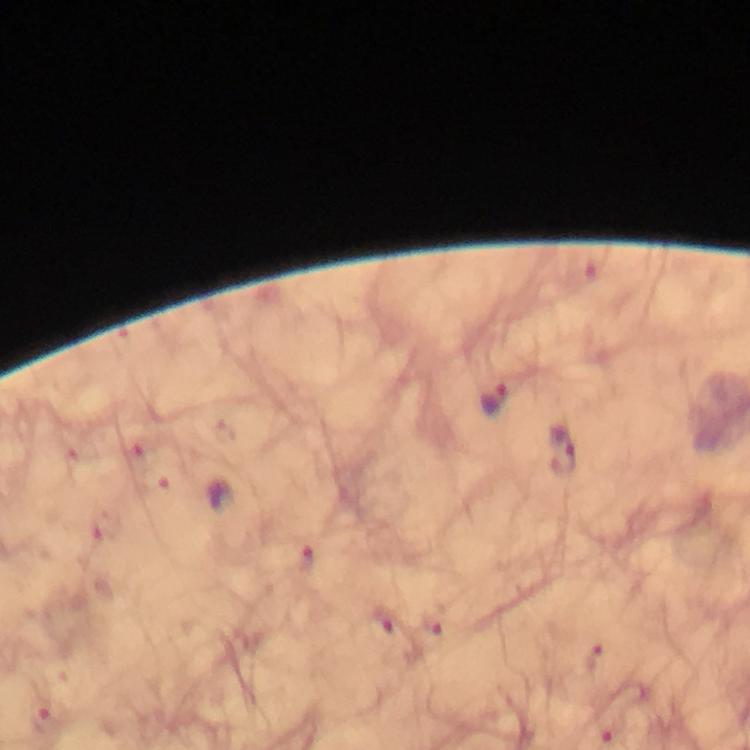

Approximate centers as (x, y) in pixels.
Summary:
  - Malaria parasite locations: (493, 400), (560, 451), (305, 560), (379, 620), (436, 625), (594, 658), (42, 723), (609, 728)
  - Cropped from: one field of view
  - Immersion oil: used
  - Context: from a diagnostic examination for malaria
  - Image size: 750×750 pixels
  - Magnification: 100x
  - Capture: smartphone photograph through a microscope
  - Preparation: thick smear
  - Stain: Giemsa